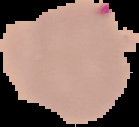

Summary:
  - Preparation: thin blood film
  - Image size: 139×127 pixels
  - Image type: segmented cell region on a black background
  - Result: malaria parasites detected